Locate every blood parasite and identify its species.
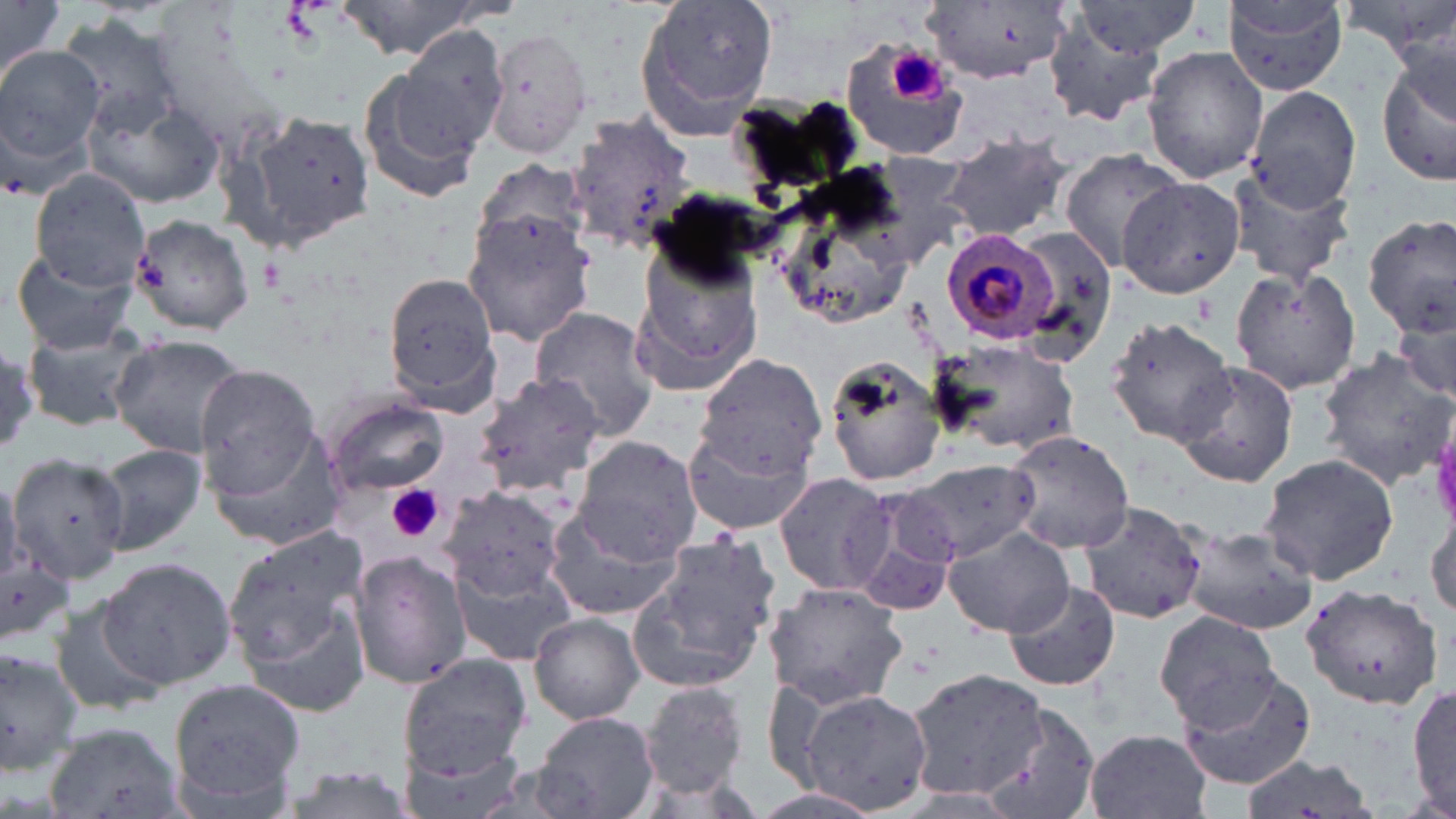
Approximate bounding boxes as (x1,y1)-(x2,y2) corner pairs in pixels.
Plasmodium malariae-infected red blood cells: (939,229)-(1060,348).
No Plasmodium falciparum, Plasmodium ovale, Plasmodium vivax, Babesia divergens, or Trypanosoma brucei observed.

Uninfected red blood cell locations: (0,0)-(64,91), (339,0)-(488,60), (630,0)-(779,139), (1225,1)-(1349,94), (920,3)-(1071,85), (1066,3)-(1206,57), (59,17)-(190,135), (1044,25)-(1166,125), (389,27)-(509,155), (483,27)-(593,161), (840,41)-(969,163), (0,43)-(106,178), (1143,47)-(1268,183), (1380,52)-(1456,190), (357,62)-(487,205), (1246,87)-(1363,214), (81,89)-(225,207), (735,97)-(853,186), (240,105)-(373,250), (567,115)-(696,250), (940,133)-(1072,242), (1058,150)-(1182,272), (854,153)-(975,265), (473,157)-(592,259), (1227,165)-(1356,287), (29,171)-(151,294), (1117,177)-(1245,297), (769,179)-(921,330), (642,188)-(775,298), (462,210)-(596,348), (128,213)-(256,336), (1360,214)-(1456,337), (1011,226)-(1118,364), (626,237)-(765,395), (9,243)-(141,358), (1230,267)-(1362,394), (381,268)-(504,414), (529,308)-(660,442), (1391,310)-(1453,408), (1106,317)-(1242,446), (23,322)-(156,432), (110,334)-(248,460), (932,338)-(1084,457), (1315,347)-(1456,489), (823,354)-(950,488), (695,356)-(828,476), (1176,361)-(1302,488), (194,363)-(328,510), (472,371)-(607,497), (324,398)-(449,497), (205,424)-(346,551), (683,427)-(814,536), (999,427)-(1135,554), (573,436)-(700,563), (94,442)-(208,555), (1259,452)-(1399,586), (8,453)-(138,581), (900,459)-(1040,564), (773,470)-(895,596), (424,483)-(573,632), (437,485)-(567,602), (846,486)-(964,612), (1076,499)-(1209,625), (1427,508)-(1456,619), (543,509)-(686,622), (1174,521)-(1319,636), (941,525)-(1077,638), (223,527)-(374,690), (641,531)-(782,684), (349,550)-(471,688), (0,555)-(74,651), (98,557)-(237,688), (453,560)-(584,667), (1002,580)-(1121,692), (763,582)-(911,710), (1301,583)-(1442,711), (45,600)-(167,718), (234,600)-(371,718), (1153,608)-(1280,732), (529,612)-(646,724), (0,651)-(80,772), (398,654)-(532,780), (1175,666)-(1317,791), (907,667)-(1045,798), (168,675)-(306,812), (634,681)-(753,798), (1410,682)-(1455,819), (794,688)-(932,815), (980,703)-(1097,819), (533,712)-(660,819), (1083,729)-(1213,819), (395,740)-(533,819), (1237,753)-(1378,819), (273,764)-(421,819). Platelet locations: (891,48)-(950,104), (385,485)-(444,544). Slide-level diagnosis: Plasmodium malariae. One field of a larger specimen. Image is 1456×819 pixels. Light microscopy. Thin blood film. May-Grünwald-Giemsa-stained preparation. 1000x magnification.